Assess this cell for malaria.
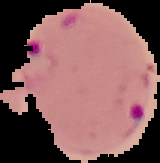
Parasitized.

Summary:
  - Image size: 160×163 pixels
  - Image type: segmented cell region on a black background
  - Preparation: thin blood film